Assess this cell for malaria.
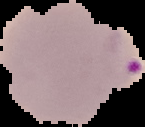
Parasitized.

{
  "image_type": "cell region segmented out of the field of view; surrounding area masked to black",
  "preparation": "thin blood film",
  "image_size": "145×127 pixels"
}